Report the malaria status of this cell.
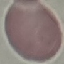

It is uninfected.

Giemsa-stained preparation. Acquired by smartphone through the microscope eyepiece. Thin smear of blood. Cell patch, automatically extracted from a larger field of view and resized to 64 × 64 pixels.